Assess the morphology of the red blood cells.
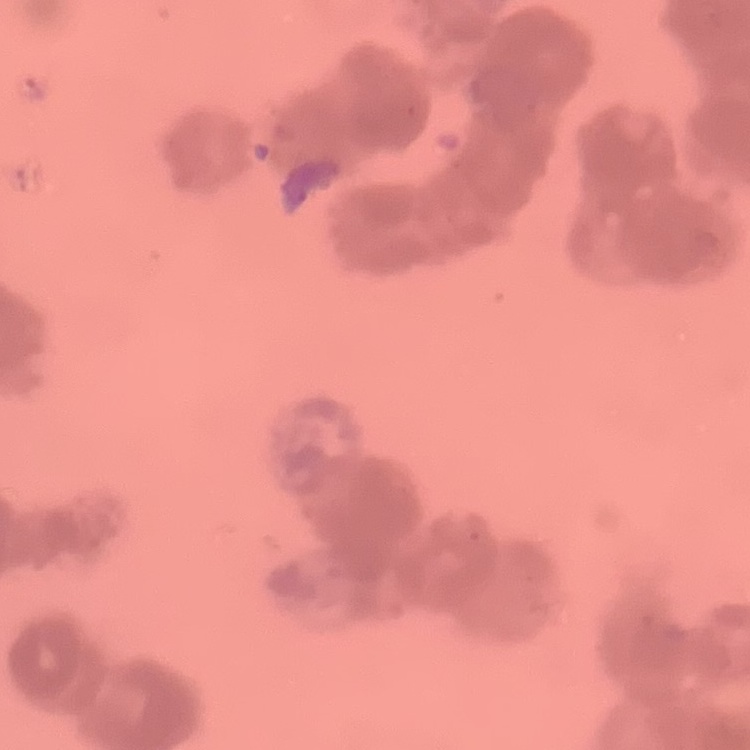
They show rouleaux formation.

preparation: thin peripheral smear
image_type: one tile cut from a larger photomicrograph
stain: Field's or Giemsa